Assess this cell for malaria.
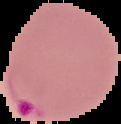
Parasitized.

Summary:
  - Preparation: thin blood smear
  - Image type: segmented cell region on a black background
  - Image size: 121×124 pixels